Comment on the morphology of the erythrocytes.
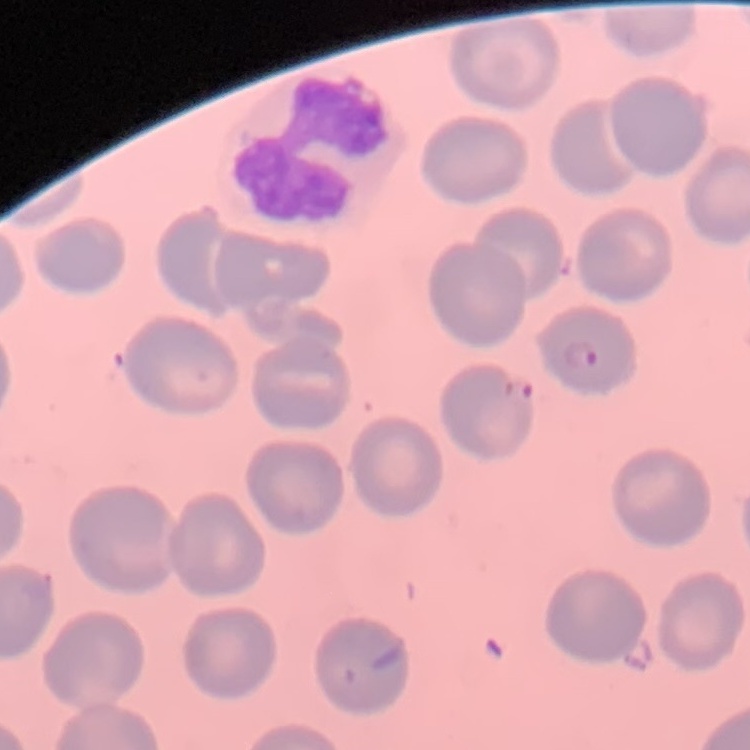

They show no rouleaux formation.

Thin peripheral smear. Field's or Giemsa stain. One tile cut from a larger photomicrograph.